Give the position of every leukocyte visible.
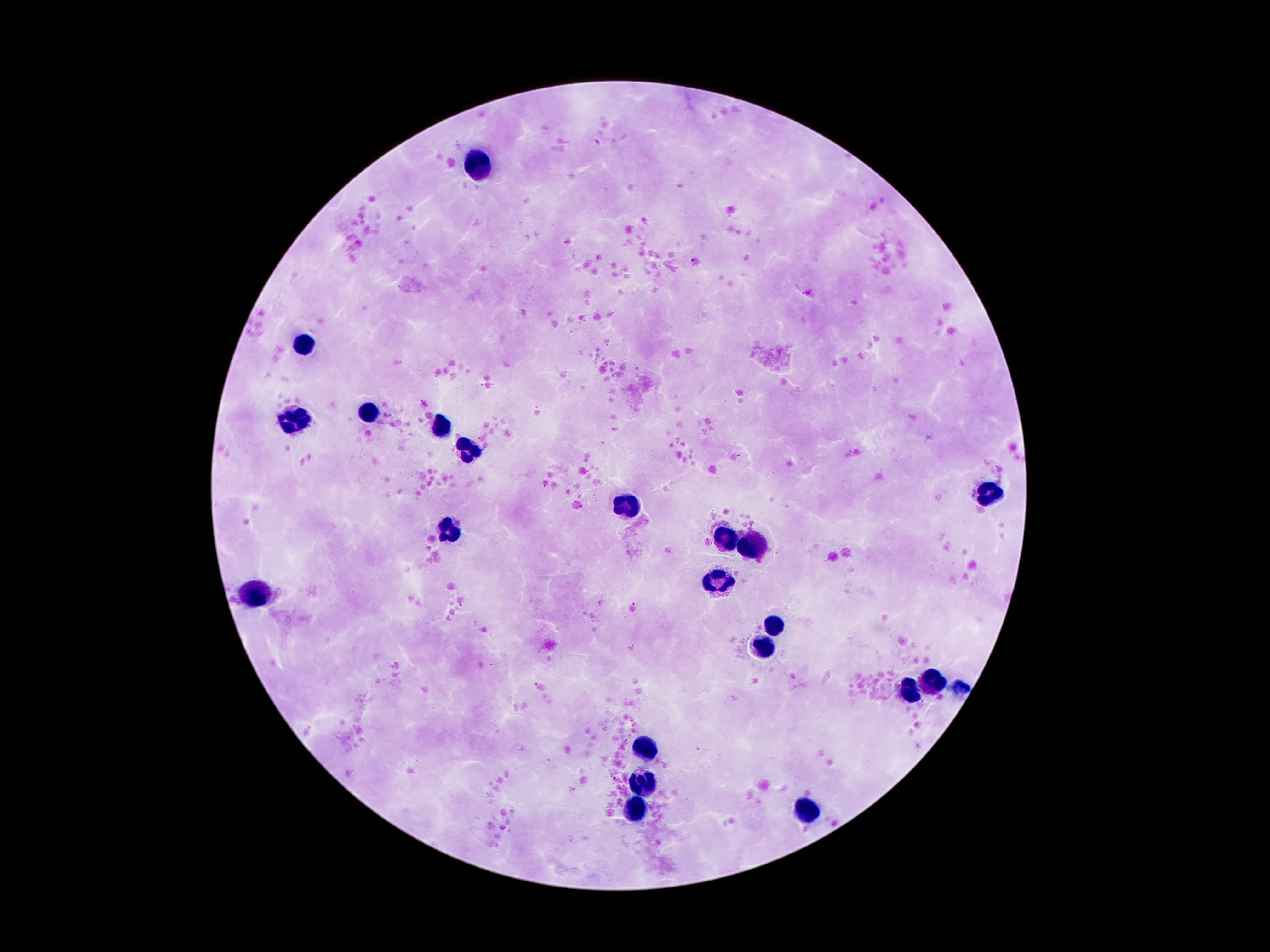
Approximate centers as {x, y} in pixels.
Leukocytes: {479, 160}, {306, 344}, {370, 412}, {292, 424}, {442, 426}, {465, 455}, {990, 492}, {626, 508}, {451, 528}, {724, 537}, {754, 546}, {722, 580}, {256, 596}, {774, 624}, {760, 644}, {931, 681}, {910, 690}, {647, 749}, {645, 780}, {638, 805}, {815, 806}.

One field from this slide. Patient malaria status: negative. Giemsa-stained preparation. Thick peripheral-blood smear. Photographed through the microscope eyepiece with a smartphone camera. 100x magnification. Image is 1270×952 pixels.